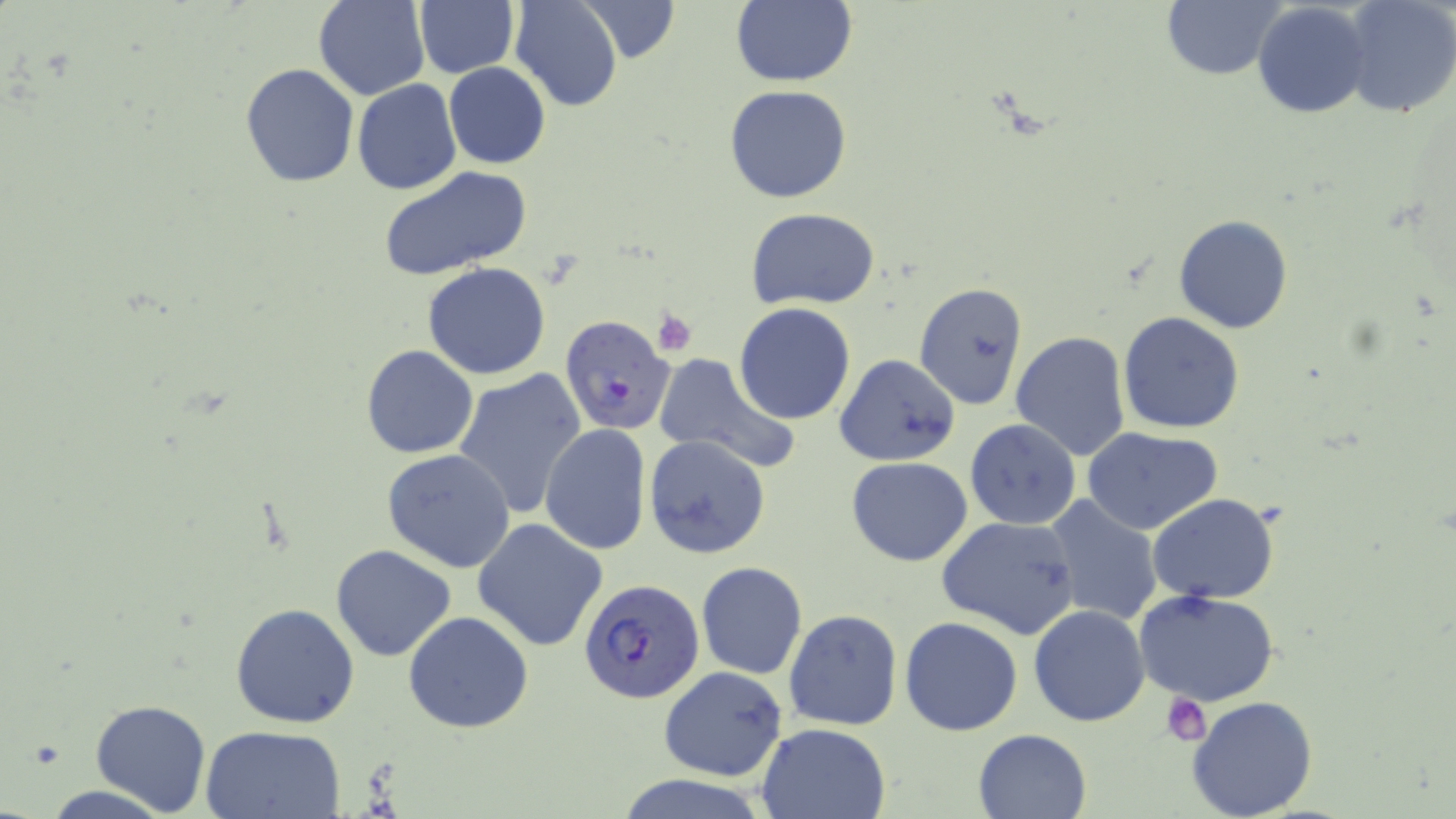

Summary:
  - Coordinate format: approximate bounding boxes as named x1/y1/x2/y2 corners in pixels
  - Plasmodium falciparum-infected red blood cell locations: (x1=560, y1=315, x2=677, y2=437), (x1=580, y1=576, x2=705, y2=704)
  - Uninfected red blood cell locations: (x1=314, y1=0, x2=431, y2=101), (x1=510, y1=0, x2=624, y2=112), (x1=576, y1=0, x2=680, y2=66), (x1=730, y1=0, x2=857, y2=87), (x1=1340, y1=0, x2=1456, y2=120), (x1=413, y1=1, x2=520, y2=79), (x1=1161, y1=1, x2=1283, y2=81), (x1=1253, y1=2, x2=1372, y2=119), (x1=240, y1=62, x2=359, y2=186), (x1=443, y1=62, x2=550, y2=169), (x1=352, y1=79, x2=461, y2=195), (x1=724, y1=84, x2=853, y2=203), (x1=356, y1=113, x2=482, y2=251), (x1=376, y1=165, x2=533, y2=281), (x1=746, y1=208, x2=882, y2=309), (x1=1174, y1=215, x2=1292, y2=334), (x1=422, y1=263, x2=551, y2=380), (x1=914, y1=281, x2=1028, y2=410), (x1=734, y1=302, x2=856, y2=425), (x1=1117, y1=311, x2=1245, y2=434), (x1=1010, y1=331, x2=1130, y2=463), (x1=361, y1=345, x2=479, y2=459), (x1=651, y1=353, x2=800, y2=474), (x1=834, y1=354, x2=962, y2=467), (x1=452, y1=368, x2=587, y2=518), (x1=965, y1=419, x2=1081, y2=531), (x1=540, y1=424, x2=651, y2=556), (x1=1081, y1=426, x2=1224, y2=533), (x1=644, y1=434, x2=771, y2=560), (x1=382, y1=449, x2=515, y2=571), (x1=846, y1=457, x2=972, y2=566), (x1=1043, y1=494, x2=1162, y2=625), (x1=1147, y1=494, x2=1279, y2=604), (x1=937, y1=516, x2=1081, y2=641), (x1=472, y1=518, x2=609, y2=652), (x1=330, y1=544, x2=456, y2=661), (x1=696, y1=561, x2=807, y2=679), (x1=1134, y1=589, x2=1282, y2=710), (x1=229, y1=603, x2=360, y2=728), (x1=1026, y1=604, x2=1151, y2=728), (x1=783, y1=609, x2=903, y2=731), (x1=403, y1=610, x2=534, y2=734), (x1=900, y1=616, x2=1022, y2=736), (x1=658, y1=666, x2=788, y2=780), (x1=1186, y1=695, x2=1319, y2=819), (x1=90, y1=700, x2=212, y2=816), (x1=756, y1=722, x2=892, y2=819), (x1=199, y1=725, x2=346, y2=818), (x1=972, y1=728, x2=1093, y2=819), (x1=33, y1=782, x2=178, y2=819)
  - Platelet locations: (x1=651, y1=308, x2=698, y2=356), (x1=1161, y1=693, x2=1211, y2=746)
  - Slide-level diagnosis: Plasmodium falciparum
  - Field of view: one of a larger specimen
  - Stain: May-Grünwald-Giemsa
  - Modality: optical microscopy
  - Image size: 1456×819 pixels
  - Magnification: 1000x
  - Preparation: thin blood film